Give the position of every Plasmodium parasite visible.
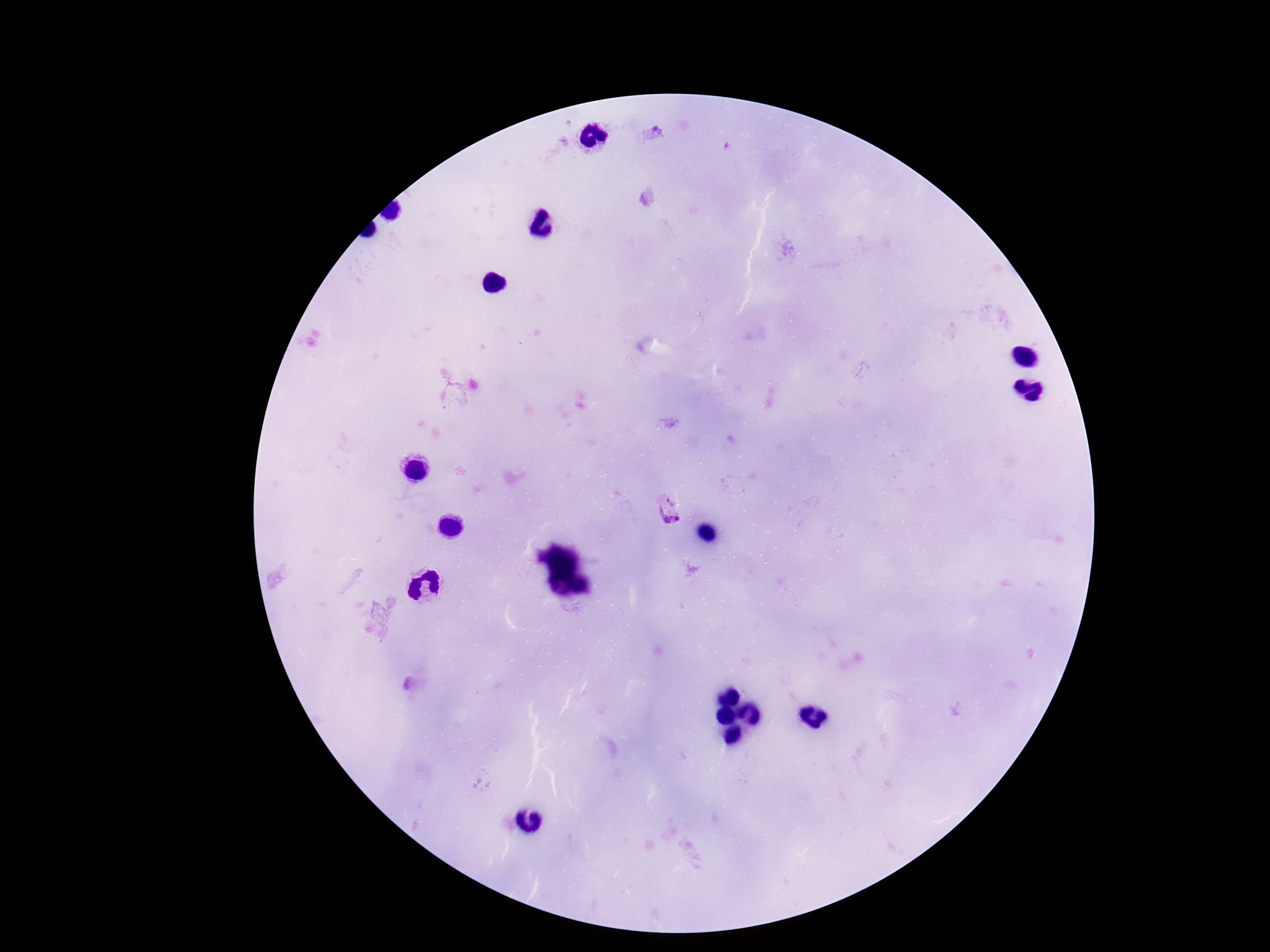
Approximate centers as (x, y) in pixels.
Plasmodium parasites: (668, 508).

Giemsa stain. Patient malaria status: positive. 100x magnification. Thick peripheral-blood smear. Image is 1270×952 pixels. Photographed through the microscope eyepiece with a smartphone camera. One field from this slide.